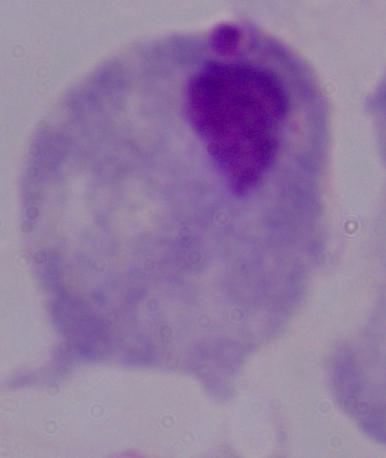
Summary:
  - Magnification: 1000x
  - Identification: trichomonad
  - Modality: micrograph